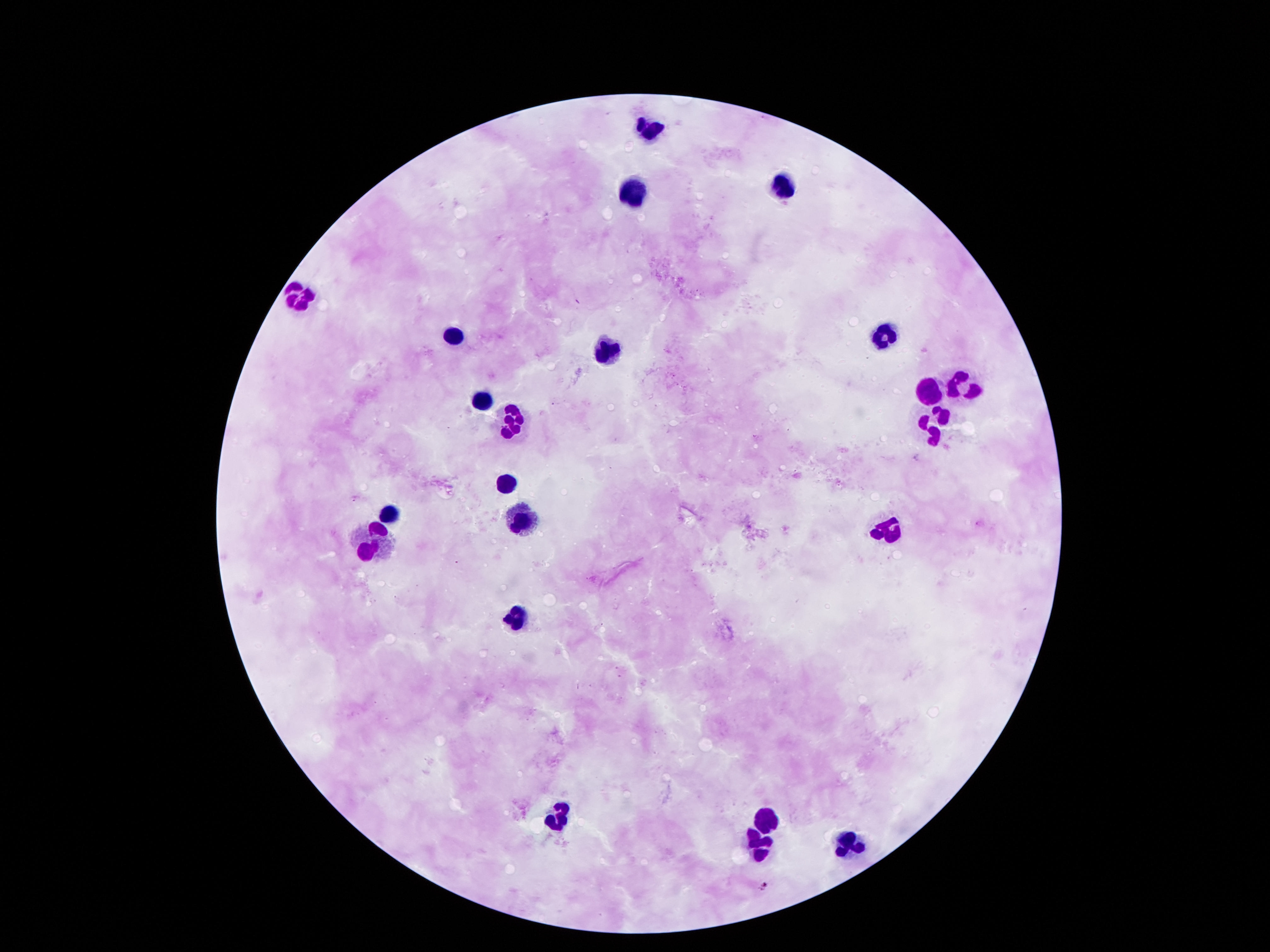
Approximate centers as [x, y] in pixels.
Summary:
  - Leukocyte locations: [654, 124], [781, 181], [634, 189], [299, 297], [878, 333], [449, 335], [608, 347], [964, 382], [929, 387], [481, 401], [514, 425], [934, 425], [506, 484], [395, 508], [520, 522], [888, 528], [370, 543], [517, 617], [557, 818], [759, 820], [851, 842], [757, 849]
  - Stain: Giemsa
  - Patient malaria status: negative
  - Magnification: 100x
  - Image size: 1270×952 pixels
  - Capture: smartphone camera through the microscope eyepiece
  - Preparation: thick peripheral-blood smear
  - Field of view: single